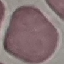

result = no malaria parasites seen
preparation = thin blood smear
stain = Giemsa
image type = cell patch, automatically extracted from a larger field of view and resized to 64 × 64 pixels
capture = smartphone camera at the microscope eyepiece